Report the malaria status of this cell.
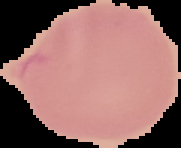

It is uninfected.

preparation = thin blood film
image type = segmented cell region with the area outside set to black
image size = 181×148 pixels